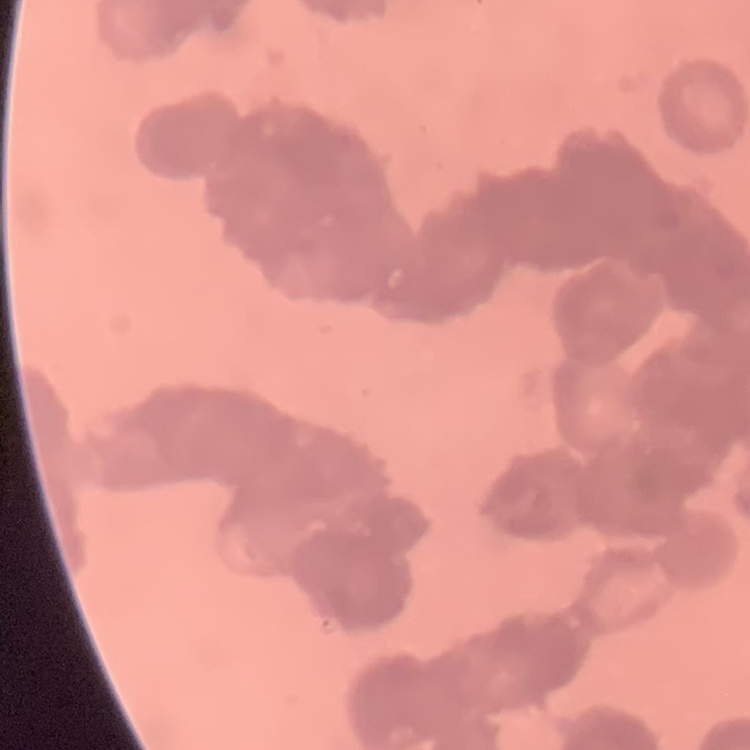

{
  "red_blood_cell_morphology": "rouleaux formation",
  "image_type": "square crop of a larger photomicrograph",
  "stain": "Field's or Giemsa",
  "preparation": "thin blood smear"
}